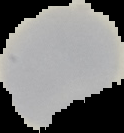
preparation = thin blood smear
image size = 124×133 pixels
result = no Plasmodium parasites seen
image type = segmented cell region on a black background